Report the malaria status of this cell.
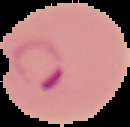

Parasitized.

preparation = thin blood film
image type = segmented cell region on a black background
image size = 130×127 pixels